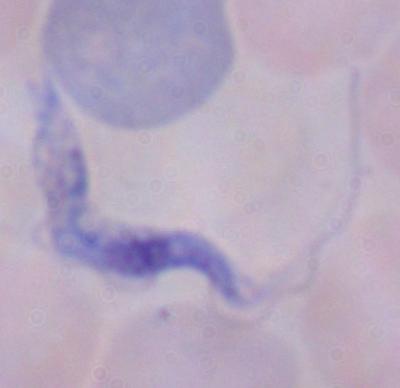 1000x magnification. Photomicrograph. A trypanosome is shown.